Assess this cell for malaria.
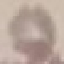
Uninfected.

preparation = thin smear
capture = smartphone through the microscope eyepiece
image type = cell patch, automatically extracted from a larger field of view and resized to 64 × 64 pixels
stain = Giemsa